Identify the blood parasite species.
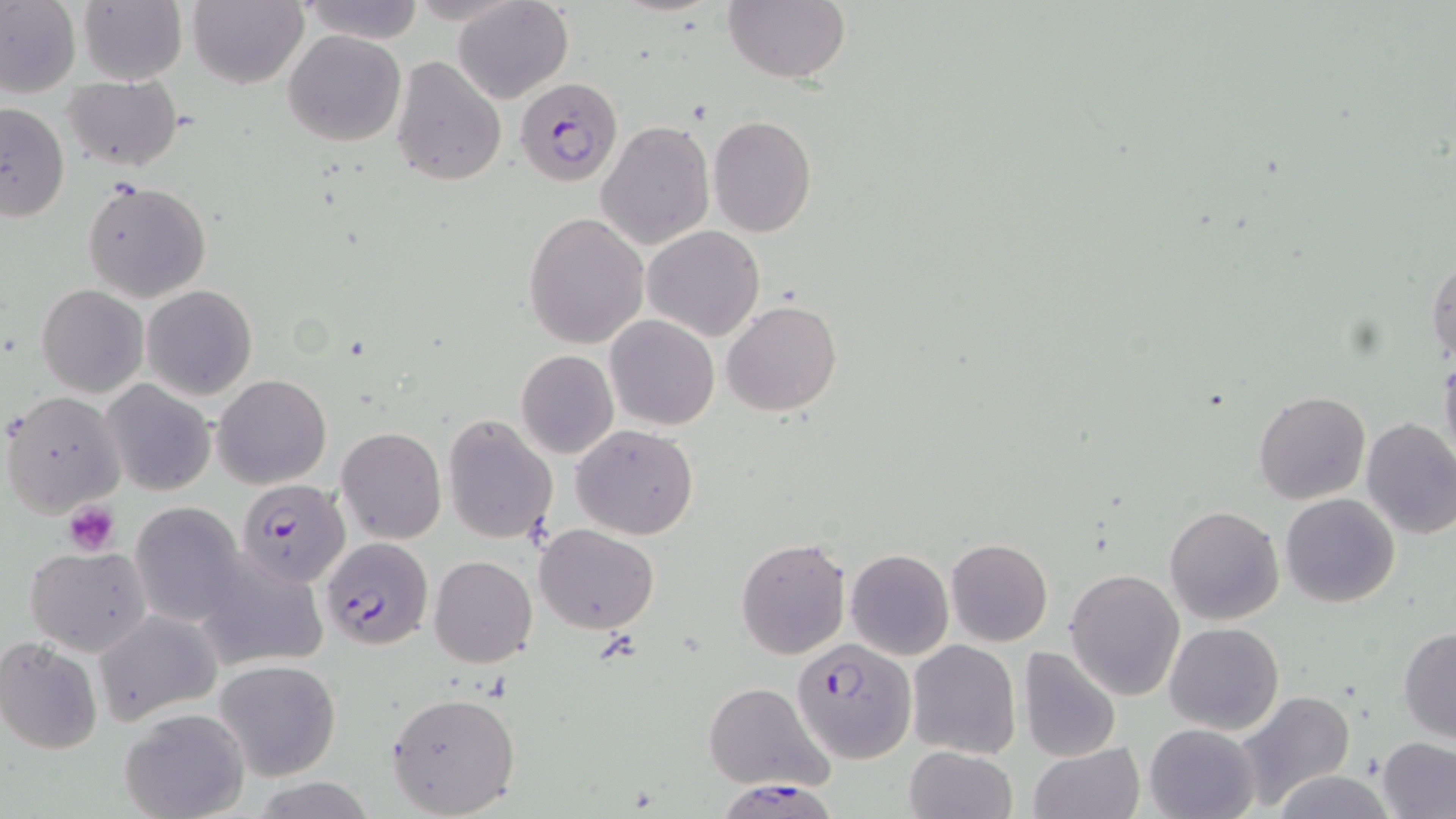
Plasmodium falciparum.

Approximate bounding boxes as named x1/y1/x2/y2 corners in pixels. Plasmodium falciparum-infected red blood cell locations: (x1=514, y1=77, x2=622, y2=186), (x1=238, y1=479, x2=350, y2=587), (x1=320, y1=535, x2=433, y2=650), (x1=791, y1=639, x2=916, y2=764), (x1=723, y1=779, x2=839, y2=819). Platelet locations: (x1=63, y1=501, x2=120, y2=557). Uninfected red blood cell locations: (x1=0, y1=0, x2=81, y2=100), (x1=79, y1=0, x2=187, y2=85), (x1=188, y1=0, x2=308, y2=89), (x1=298, y1=0, x2=425, y2=43), (x1=453, y1=0, x2=574, y2=105), (x1=723, y1=0, x2=850, y2=84), (x1=283, y1=29, x2=407, y2=147), (x1=389, y1=55, x2=508, y2=188), (x1=63, y1=74, x2=184, y2=169), (x1=0, y1=101, x2=69, y2=223), (x1=706, y1=115, x2=816, y2=237), (x1=596, y1=119, x2=715, y2=251), (x1=82, y1=179, x2=211, y2=302), (x1=523, y1=212, x2=650, y2=348), (x1=641, y1=225, x2=765, y2=342), (x1=1426, y1=251, x2=1456, y2=368), (x1=37, y1=285, x2=148, y2=396), (x1=141, y1=285, x2=257, y2=400), (x1=722, y1=300, x2=841, y2=416), (x1=606, y1=316, x2=720, y2=430), (x1=515, y1=350, x2=620, y2=460), (x1=1439, y1=351, x2=1456, y2=467), (x1=214, y1=374, x2=331, y2=488), (x1=102, y1=380, x2=215, y2=495), (x1=1253, y1=390, x2=1371, y2=504), (x1=2, y1=391, x2=124, y2=516), (x1=443, y1=415, x2=558, y2=543), (x1=1359, y1=418, x2=1456, y2=539), (x1=571, y1=424, x2=698, y2=539), (x1=336, y1=427, x2=447, y2=545), (x1=1280, y1=492, x2=1400, y2=607), (x1=129, y1=502, x2=246, y2=626), (x1=1163, y1=505, x2=1285, y2=625), (x1=535, y1=524, x2=658, y2=634), (x1=735, y1=538, x2=851, y2=659), (x1=944, y1=538, x2=1053, y2=646), (x1=23, y1=544, x2=152, y2=655), (x1=846, y1=548, x2=953, y2=659), (x1=194, y1=552, x2=329, y2=673), (x1=428, y1=555, x2=537, y2=668), (x1=1064, y1=568, x2=1184, y2=701), (x1=92, y1=609, x2=223, y2=725), (x1=1164, y1=622, x2=1284, y2=734), (x1=1398, y1=627, x2=1456, y2=743), (x1=0, y1=637, x2=102, y2=754), (x1=907, y1=638, x2=1021, y2=758), (x1=1018, y1=644, x2=1123, y2=760), (x1=214, y1=658, x2=341, y2=781), (x1=702, y1=683, x2=831, y2=791), (x1=1232, y1=690, x2=1357, y2=810), (x1=387, y1=691, x2=522, y2=817), (x1=118, y1=706, x2=251, y2=819), (x1=1145, y1=722, x2=1262, y2=819), (x1=1377, y1=738, x2=1456, y2=819), (x1=1030, y1=742, x2=1141, y2=819), (x1=903, y1=745, x2=1017, y2=819), (x1=1270, y1=771, x2=1395, y2=818). One field of a larger specimen. May-Grünwald-Giemsa stain. Optical microscopy. Thin blood film. Image is 1456×819 pixels. 1000x magnification.